Classify this cell by malaria status.
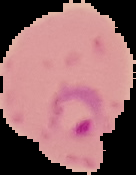

It is parasitized.

From a thin blood smear. Image is 136×175 pixels. Cell region segmented out of the field of view; the surrounding area is masked to black.